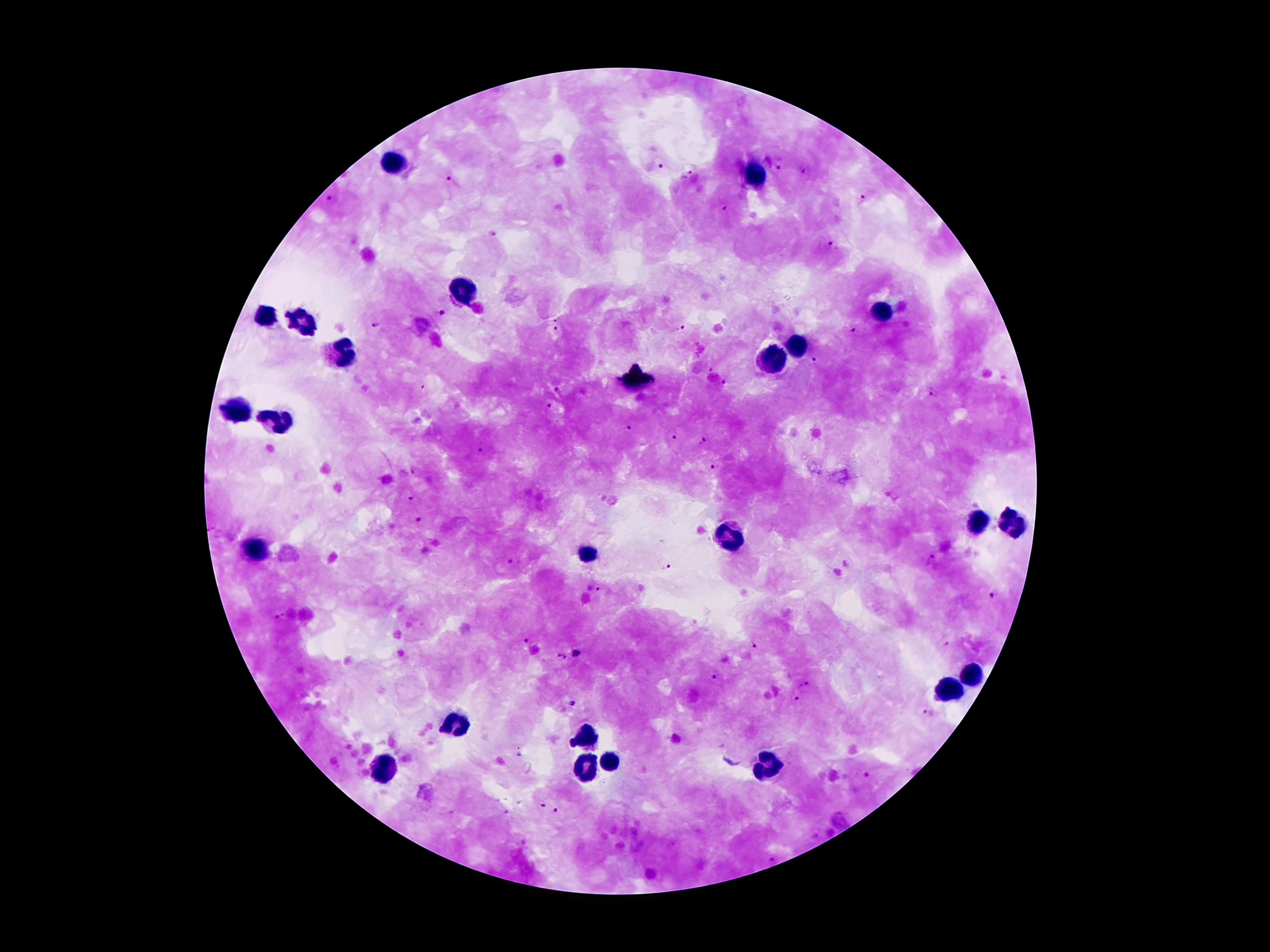
coordinate format = approximate centers as {x, y} in pixels
leukocyte locations = {397, 162}, {754, 178}, {463, 292}, {879, 310}, {269, 317}, {303, 324}, {799, 347}, {339, 352}, {770, 360}, {235, 414}, {277, 423}, {979, 523}, {1013, 523}, {733, 537}, {259, 552}, {584, 552}, {973, 679}, {945, 692}, {455, 722}, {585, 739}, {609, 760}, {587, 764}, {387, 768}, {767, 768}
Plasmodium parasite locations = {658, 164}, {780, 166}, {806, 170}, {687, 175}, {450, 178}, {331, 198}, {861, 198}, {724, 207}, {493, 234}, {829, 243}, {441, 311}, {555, 317}, {377, 324}, {680, 328}, {555, 329}, {856, 334}, {814, 360}, {724, 381}, {556, 389}, {934, 393}, {549, 404}, {628, 428}, {673, 436}, {706, 439}, {482, 448}, {714, 466}, {415, 499}, {419, 520}, {514, 561}, {932, 561}, {663, 563}, {601, 588}, {995, 594}, {278, 617}, {527, 640}, {754, 643}, {945, 644}, {558, 653}, {577, 653}, {566, 658}, {715, 678}, {804, 687}, {797, 702}, {573, 704}, {926, 712}, {867, 776}, {542, 802}, {556, 811}, {771, 858}
image size = 1270×952 pixels
preparation = thick peripheral-blood smear
magnification = 100x
patient malaria status = positive for Plasmodium falciparum
stain = Giemsa
field of view = single
capture = smartphone camera through the microscope eyepiece